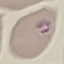
Malaria status: parasitized. Giemsa-stained preparation. Thin smear of blood. Acquired by smartphone through the microscope eyepiece. Automatically extracted cell patch, resized to 64 × 64 pixels.